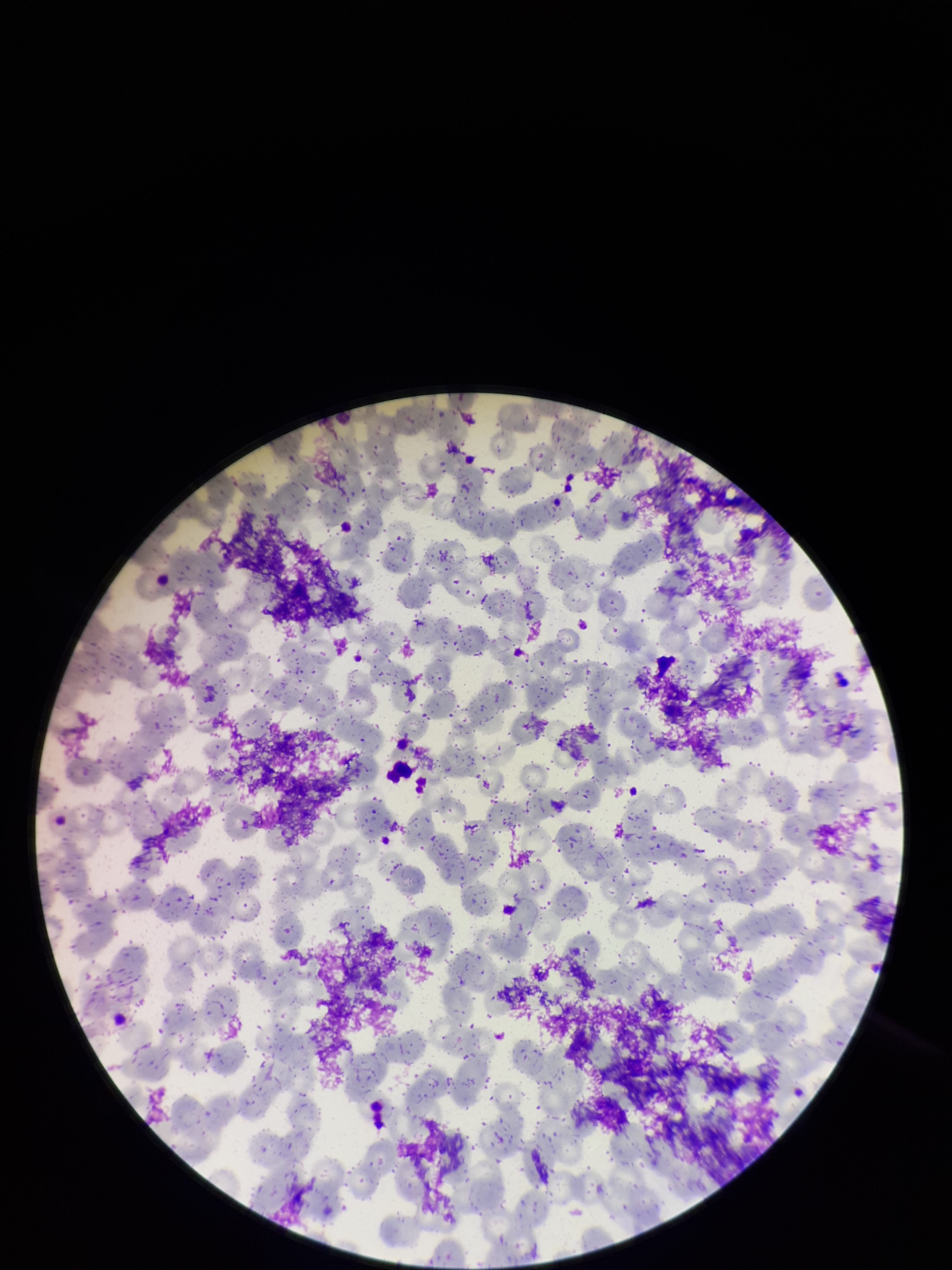

Single field of view. Photographed through the microscope eyepiece with a smartphone camera. Parasitized red blood cells: none seen. Image is 952×1270 pixels. Red blood cell count: 300. Parasitized red blood cell count: 0. Patient malaria status: negative. Giemsa stain. Preparation: thin.